Name the parasite shown.
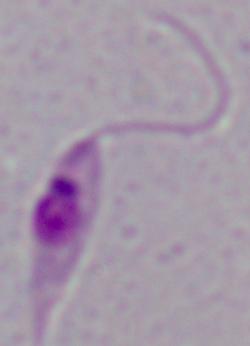

This is Leishmania.

modality = micrograph
magnification = 1000x